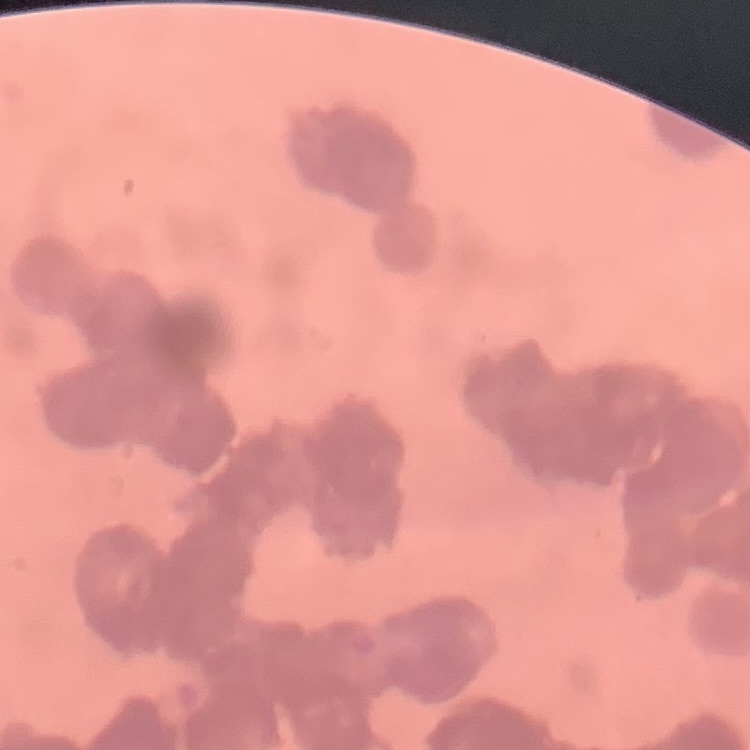

The erythrocytes show rouleaux formation. One tile cut from a larger photomicrograph. Thin blood film. Field's or Giemsa stain.